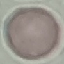
Summary:
  - Malaria status: uninfected
  - Stain: Giemsa
  - Preparation: thin blood smear
  - Capture: smartphone through the microscope eyepiece
  - Image type: automatically extracted cell patch, resized to 64 × 64 pixels